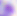
Summary:
  - Magnification: 400x
  - Modality: micrograph
  - Identification: Toxoplasma gondii